Assess this cell for malaria.
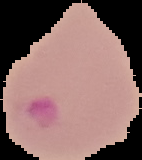
Parasitized.

Summary:
  - Image type: cell region segmented out of the field of view; surrounding area masked to black
  - Preparation: thin blood smear
  - Image size: 142×160 pixels